Classify this cell by malaria status.
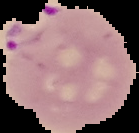
It is parasitized.

Summary:
  - Image type: cell region segmented out of the field of view; surrounding area masked to black
  - Image size: 139×133 pixels
  - Preparation: thin blood film